Outline each blood parasite and name the species.
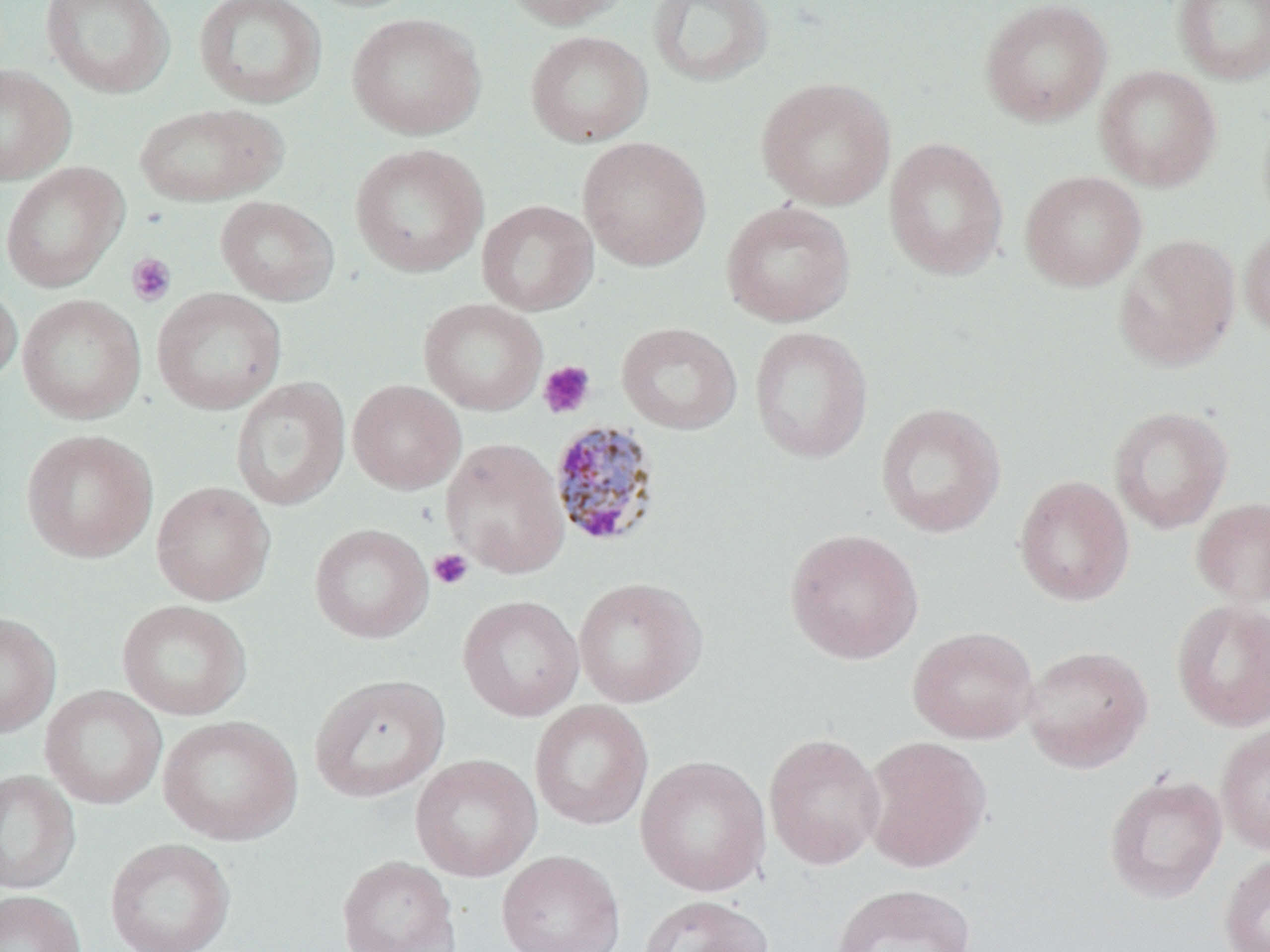
Approximate bounding boxes as named x1/y1/x2/y2 corners in pixels.
Plasmodium malariae-infected red blood cells: (x1=549, y1=420, x2=661, y2=549).
No Plasmodium falciparum, Plasmodium ovale, Plasmodium vivax, Babesia divergens, or Trypanosoma brucei observed.

Summary:
  - Platelet locations: (x1=126, y1=253, x2=176, y2=307), (x1=537, y1=360, x2=596, y2=419), (x1=429, y1=548, x2=474, y2=590)
  - Uninfected red blood cell locations: (x1=40, y1=0, x2=175, y2=98), (x1=193, y1=0, x2=327, y2=108), (x1=498, y1=0, x2=633, y2=29), (x1=647, y1=0, x2=774, y2=87), (x1=979, y1=0, x2=1112, y2=127), (x1=1172, y1=0, x2=1270, y2=85), (x1=346, y1=12, x2=486, y2=139), (x1=525, y1=31, x2=652, y2=147), (x1=0, y1=64, x2=76, y2=186), (x1=1095, y1=65, x2=1222, y2=191), (x1=756, y1=77, x2=896, y2=210), (x1=133, y1=103, x2=286, y2=206), (x1=577, y1=136, x2=711, y2=271), (x1=884, y1=138, x2=1008, y2=280), (x1=349, y1=143, x2=489, y2=278), (x1=0, y1=162, x2=128, y2=293), (x1=1020, y1=170, x2=1146, y2=292), (x1=215, y1=196, x2=339, y2=305), (x1=477, y1=200, x2=598, y2=316), (x1=721, y1=201, x2=855, y2=327), (x1=1239, y1=224, x2=1270, y2=339), (x1=1114, y1=234, x2=1241, y2=372), (x1=0, y1=279, x2=22, y2=389), (x1=152, y1=288, x2=287, y2=415), (x1=17, y1=294, x2=146, y2=424), (x1=418, y1=298, x2=547, y2=416), (x1=617, y1=322, x2=742, y2=434), (x1=749, y1=326, x2=873, y2=463), (x1=231, y1=377, x2=351, y2=511), (x1=348, y1=380, x2=465, y2=494), (x1=875, y1=402, x2=1007, y2=539), (x1=1108, y1=406, x2=1233, y2=533), (x1=21, y1=429, x2=158, y2=563), (x1=441, y1=438, x2=570, y2=579), (x1=1013, y1=475, x2=1134, y2=607), (x1=152, y1=481, x2=275, y2=606), (x1=1191, y1=497, x2=1270, y2=608), (x1=309, y1=523, x2=433, y2=644), (x1=784, y1=528, x2=924, y2=664), (x1=572, y1=577, x2=707, y2=708), (x1=458, y1=595, x2=584, y2=721), (x1=1170, y1=598, x2=1270, y2=731), (x1=117, y1=600, x2=252, y2=720), (x1=0, y1=612, x2=61, y2=738), (x1=907, y1=626, x2=1040, y2=744), (x1=1021, y1=644, x2=1153, y2=773), (x1=309, y1=673, x2=450, y2=802), (x1=40, y1=685, x2=167, y2=809), (x1=529, y1=700, x2=653, y2=831), (x1=158, y1=715, x2=302, y2=845), (x1=1216, y1=721, x2=1270, y2=856), (x1=763, y1=732, x2=885, y2=869), (x1=862, y1=736, x2=992, y2=873), (x1=410, y1=754, x2=542, y2=881), (x1=635, y1=755, x2=771, y2=897), (x1=0, y1=769, x2=80, y2=894), (x1=1103, y1=774, x2=1227, y2=904), (x1=105, y1=837, x2=236, y2=952), (x1=496, y1=849, x2=626, y2=952), (x1=1218, y1=853, x2=1270, y2=952), (x1=336, y1=855, x2=460, y2=952), (x1=829, y1=882, x2=976, y2=952), (x1=0, y1=890, x2=86, y2=952), (x1=638, y1=894, x2=774, y2=952)
  - Slide-level diagnosis: Plasmodium malariae
  - Field of view: one of a larger specimen
  - Magnification: 1000x
  - Preparation: thin blood smear
  - Modality: optical microscopy
  - Image size: 1270×952 pixels
  - Stain: May-Grünwald-Giemsa